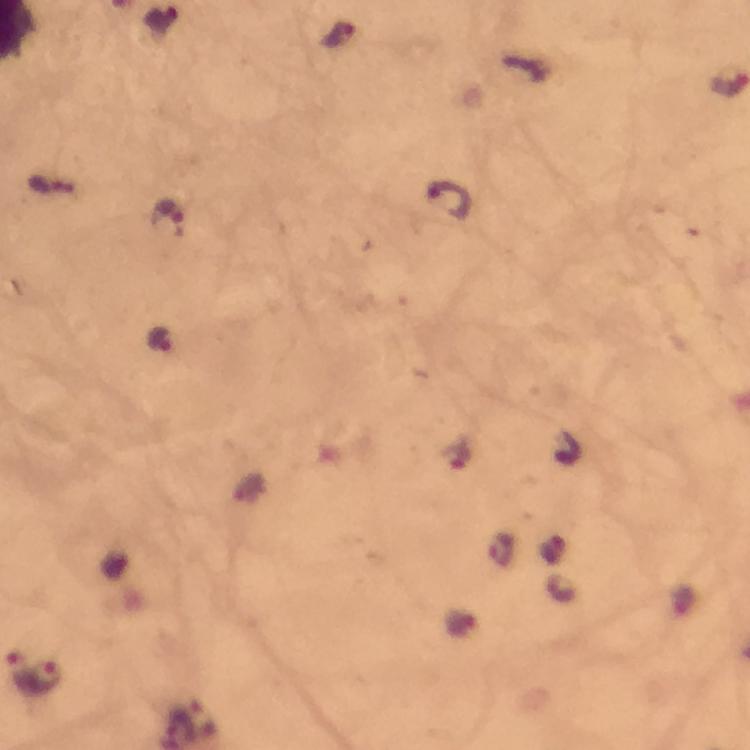
Approximate centers as (x, y) in pixels.
Summary:
  - Malaria parasite locations: (448, 200), (171, 218), (161, 338), (19, 670), (46, 675)
  - Capture: smartphone camera through the microscope
  - Context: from a diagnostic examination for malaria
  - Cropped from: one field of view
  - Stain: Giemsa
  - Image size: 750×750 pixels
  - Preparation: thick blood film
  - Immersion oil: used
  - Magnification: 100x